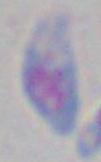

Photomicrograph. Toxoplasma gondii is shown. 1000x magnification.